Give the position of every malaria parasite and every leukocyte.
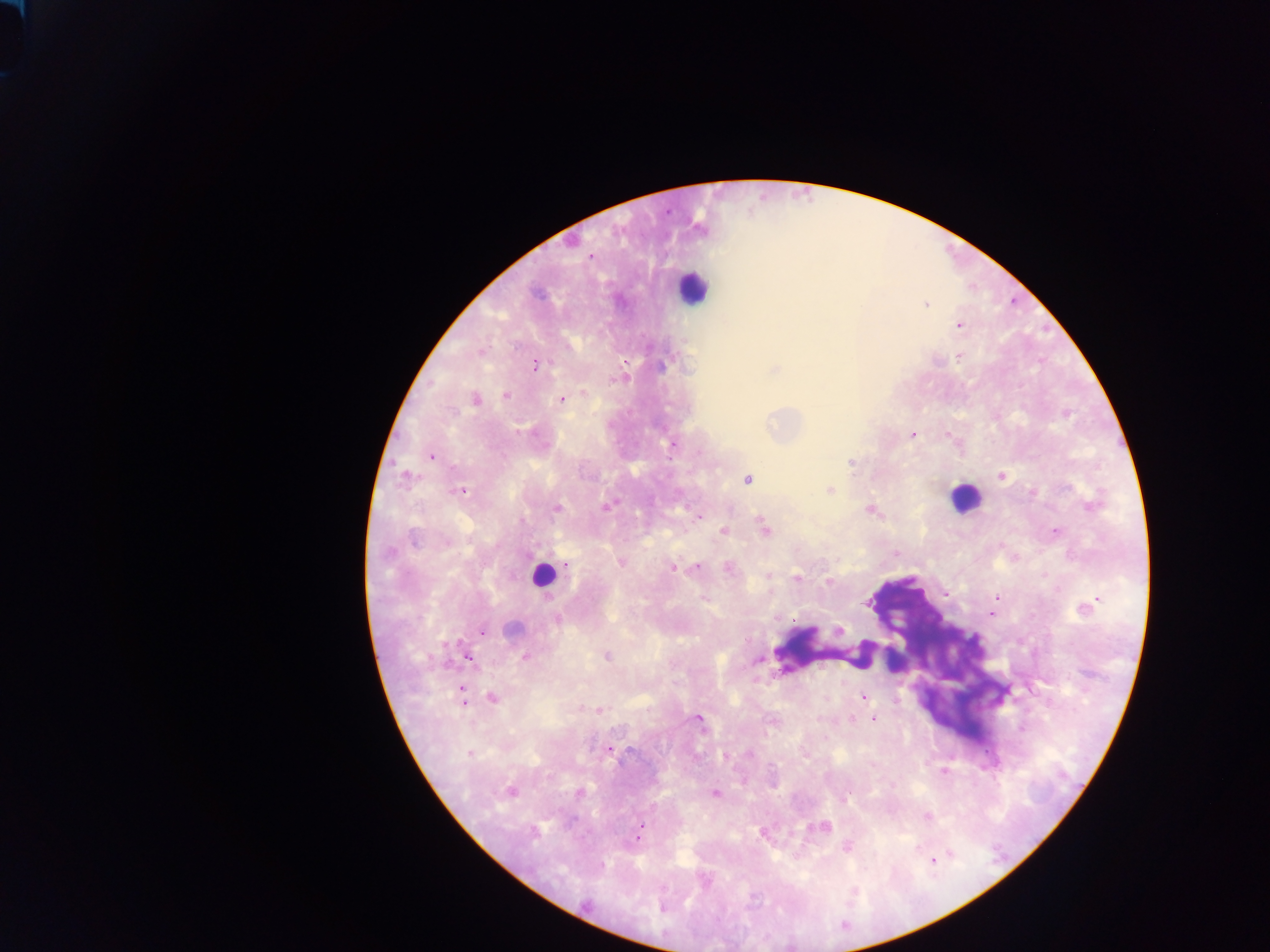

Approximate centers as x y in pixels.
Malaria parasites: 591 256; 926 304; 959 325; 959 357; 535 365; 662 365; 774 370; 616 379; 584 394; 505 396; 475 399; 562 400; 912 435; 672 444; 430 457; 852 463; 405 476; 1001 476; 748 479; 829 490; 461 491; 1090 506; 606 507; 557 508; 870 510; 700 516; 764 528; 723 532; 1055 532; 414 541; 620 562; 567 564; 697 567; 728 567; 673 568; 768 575; 797 577; 828 582; 997 596; 995 602; 867 603; 1087 607; 991 613; 558 618; 513 628; 839 630; 483 632; 606 656; 525 657; 468 658; 758 661; 462 692; 864 697; 492 698; 599 711; 852 718; 874 719; 699 720; 610 749; 469 753; 749 754; 804 756; 944 770; 511 792; 579 793; 715 793; 846 796; 927 817; 641 827; 824 828; 533 832; 638 836; 847 847; 934 861; 662 908.
Leukocytes: 692 287; 964 497; 543 576.

preparation = thick blood film
field of view = single
capture = mobile-phone photograph through a microscope
country = Ghana
image size = 1270×952 pixels